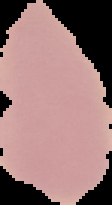

Result: negative for malaria parasites. Segmented cell region on a black background. From a thin blood smear. Image is 112×205 pixels.